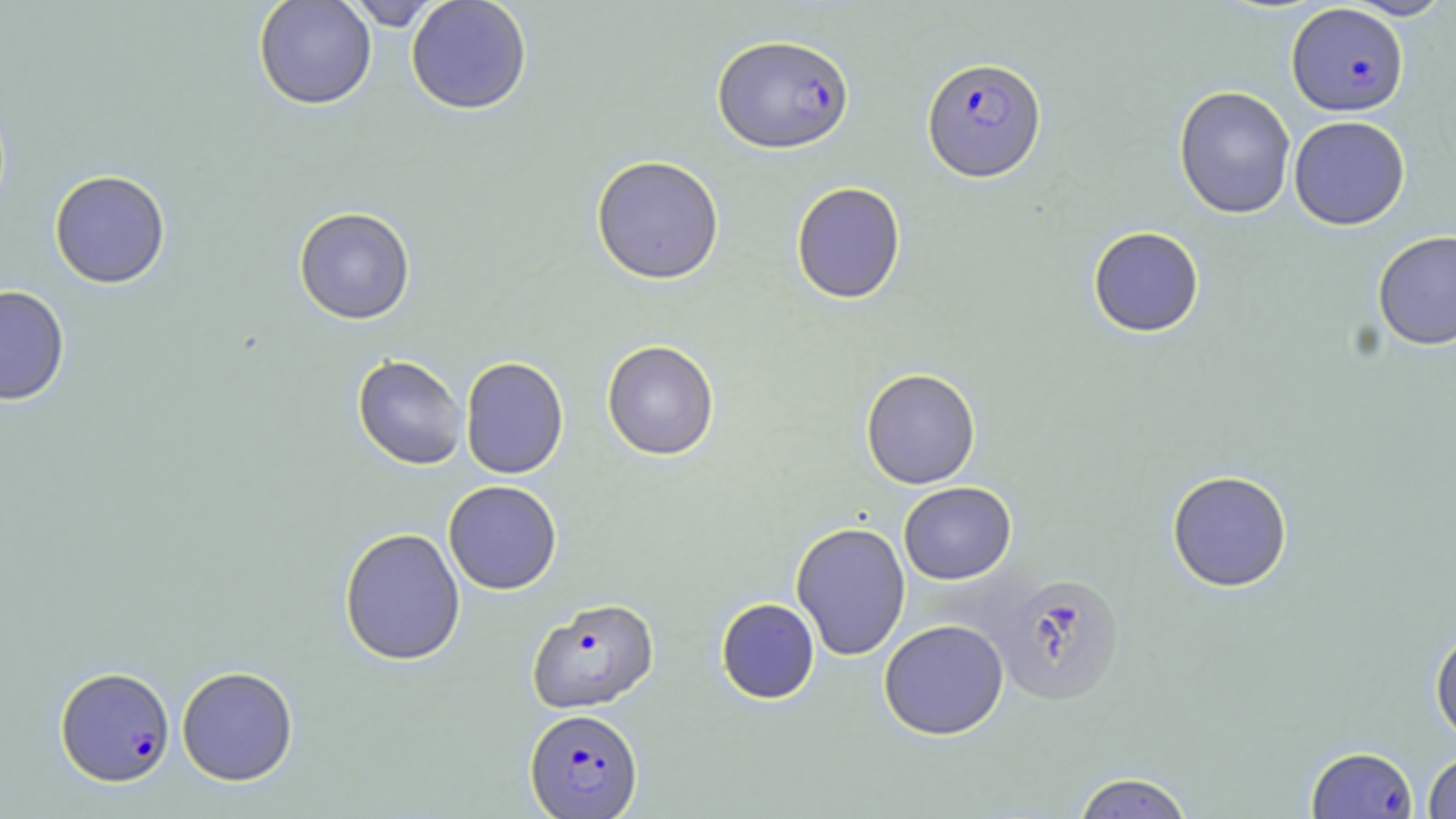

Summary:
  - Coordinate format: approximate bounding boxes as (x1, y1, x2, y2) in pixels
  - Uninfected red blood cell locations: (253, 0, 377, 110), (342, 0, 446, 30), (406, 0, 532, 114), (1343, 0, 1453, 20), (1173, 85, 1296, 219), (1288, 115, 1410, 230), (590, 154, 725, 284), (49, 169, 171, 288), (790, 182, 906, 304), (293, 207, 416, 324), (1087, 226, 1205, 338), (1372, 230, 1456, 351), (0, 284, 71, 406), (602, 339, 720, 460), (352, 354, 468, 469), (460, 356, 569, 479), (860, 368, 981, 489), (1166, 469, 1293, 592), (443, 480, 562, 595), (899, 481, 1017, 584), (790, 521, 911, 661), (339, 527, 466, 666), (990, 570, 1127, 706), (715, 598, 820, 704), (878, 619, 1009, 740), (1430, 626, 1456, 744), (177, 665, 298, 786), (1422, 750, 1456, 818), (1071, 771, 1196, 818)
  - Plasmodium falciparum-infected red blood cell locations: (1286, 3, 1409, 117), (712, 33, 854, 154), (921, 56, 1047, 182), (528, 597, 659, 713), (55, 665, 175, 786), (525, 708, 643, 817), (1306, 745, 1418, 819)
  - Slide-level diagnosis: Plasmodium falciparum
  - Stain: May-Grünwald-Giemsa
  - Magnification: 1000x
  - Field of view: one of a larger specimen
  - Modality: light microscopy
  - Image size: 1456×819 pixels
  - Preparation: thin blood film